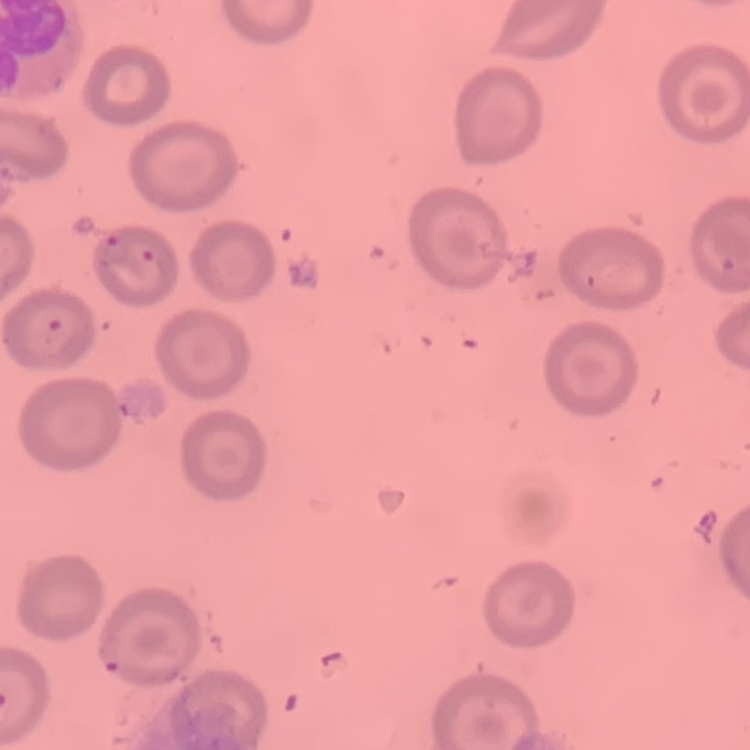 The red blood cells show no rouleaux formation. Square crop of a larger photomicrograph. Field's or Giemsa stain. Thin blood smear.